Locate every parasitized red blood cell.
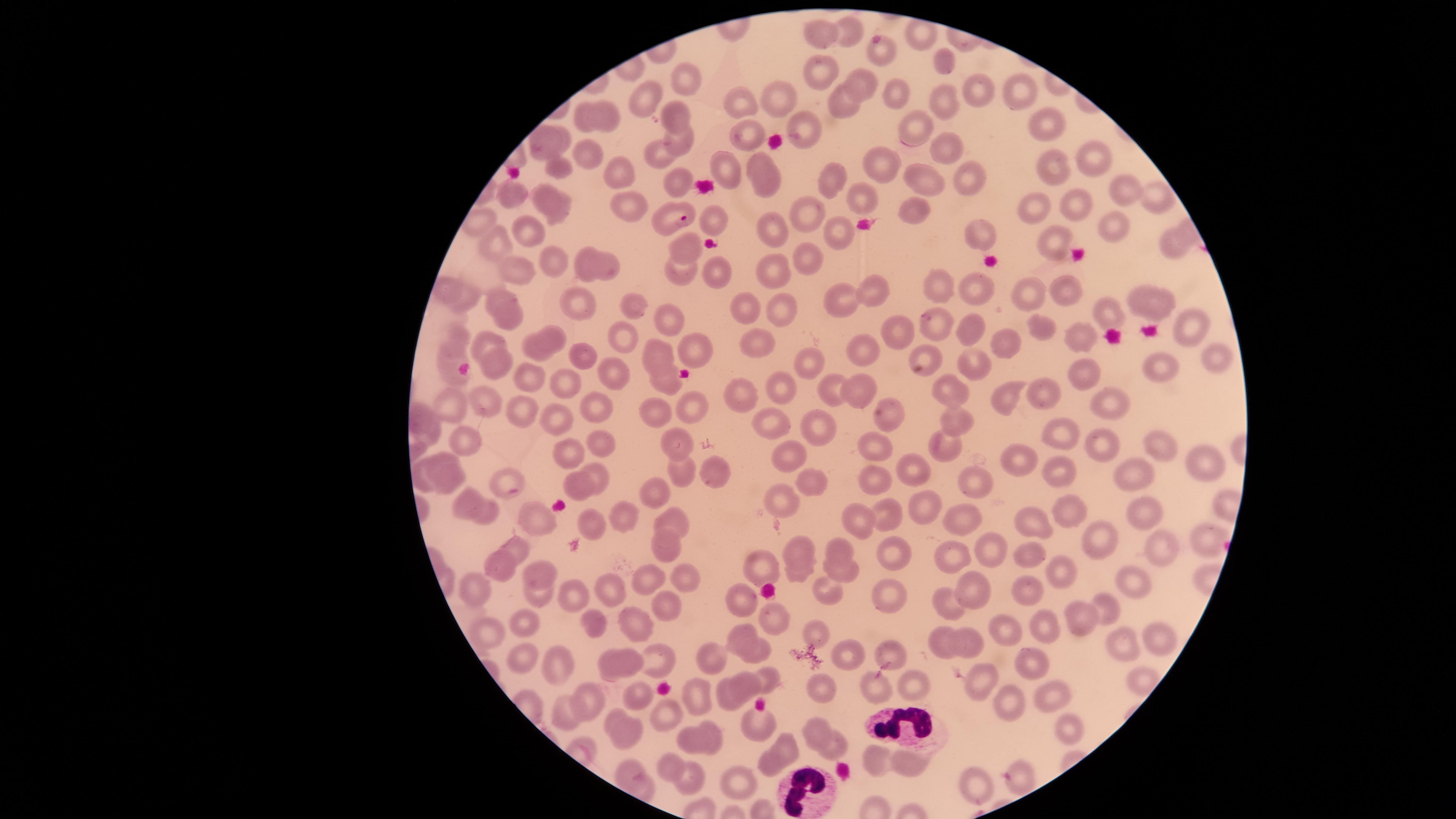
Approximate marker points, in pixels from the top-left corner.
Parasitized red blood cells: (x=668, y=215).

Approximate marker points, in pixels from the top-left corner. White blood cells: (x=901, y=723), (x=806, y=794). Uninfected red blood cells: (x=821, y=32), (x=849, y=35), (x=884, y=56), (x=939, y=62), (x=823, y=72), (x=688, y=77), (x=866, y=84), (x=1017, y=86), (x=973, y=87), (x=896, y=92), (x=645, y=94), (x=776, y=94), (x=745, y=101), (x=946, y=104), (x=846, y=106), (x=670, y=111), (x=582, y=116), (x=611, y=119), (x=917, y=121), (x=1045, y=125), (x=747, y=131), (x=562, y=132), (x=677, y=135), (x=803, y=135), (x=591, y=147), (x=544, y=149), (x=658, y=151), (x=946, y=152), (x=1086, y=152), (x=759, y=160), (x=883, y=167), (x=728, y=168), (x=1055, y=170), (x=622, y=173), (x=562, y=174), (x=833, y=174), (x=976, y=176), (x=925, y=180), (x=683, y=181), (x=768, y=182), (x=1124, y=187), (x=551, y=193), (x=1147, y=193), (x=518, y=194), (x=862, y=201), (x=1081, y=204), (x=623, y=205), (x=915, y=212), (x=808, y=213), (x=1038, y=213), (x=564, y=216), (x=711, y=220), (x=847, y=226), (x=1114, y=228), (x=771, y=229), (x=529, y=231), (x=983, y=238), (x=500, y=241), (x=1172, y=244), (x=1059, y=245), (x=688, y=250), (x=586, y=255), (x=548, y=256), (x=813, y=262), (x=607, y=271), (x=680, y=271), (x=518, y=273), (x=717, y=274), (x=771, y=275), (x=938, y=283), (x=981, y=289), (x=1065, y=289), (x=877, y=291), (x=500, y=293), (x=1034, y=293), (x=469, y=298), (x=1142, y=298), (x=1168, y=303), (x=851, y=304), (x=580, y=308), (x=742, y=308), (x=635, y=310), (x=779, y=311), (x=517, y=312), (x=1111, y=314), (x=670, y=317), (x=969, y=328), (x=1042, y=328), (x=1188, y=328), (x=934, y=329), (x=890, y=334), (x=558, y=335), (x=1082, y=335), (x=629, y=336), (x=458, y=341), (x=488, y=341), (x=1004, y=343), (x=763, y=345), (x=537, y=346), (x=705, y=350), (x=653, y=352), (x=929, y=353), (x=579, y=354), (x=861, y=354), (x=502, y=356), (x=808, y=358), (x=1218, y=362), (x=974, y=365), (x=1161, y=367), (x=449, y=368), (x=618, y=373), (x=528, y=374), (x=1086, y=381), (x=569, y=382), (x=665, y=383), (x=783, y=387), (x=945, y=388), (x=830, y=389), (x=858, y=390), (x=742, y=396), (x=1009, y=396), (x=1045, y=397), (x=480, y=399), (x=1112, y=404), (x=455, y=405), (x=597, y=405), (x=694, y=407), (x=659, y=409), (x=523, y=411), (x=556, y=413), (x=955, y=417), (x=889, y=418), (x=423, y=419), (x=772, y=422), (x=817, y=424), (x=1069, y=435), (x=941, y=438), (x=674, y=439), (x=469, y=441), (x=603, y=441), (x=873, y=443), (x=1097, y=443), (x=1159, y=449), (x=572, y=452), (x=783, y=454), (x=443, y=458), (x=1203, y=459), (x=1022, y=465), (x=919, y=467), (x=677, y=468), (x=1057, y=468), (x=1137, y=470), (x=419, y=474), (x=589, y=474), (x=714, y=475), (x=873, y=478), (x=976, y=481), (x=445, y=483), (x=811, y=483), (x=513, y=484), (x=582, y=488), (x=654, y=491), (x=465, y=501), (x=780, y=502), (x=885, y=511), (x=929, y=511), (x=1145, y=511), (x=1067, y=513), (x=490, y=515), (x=616, y=515), (x=964, y=517), (x=535, y=518), (x=858, y=518), (x=672, y=519), (x=1035, y=525), (x=590, y=528), (x=1098, y=538), (x=1207, y=540), (x=660, y=545), (x=837, y=546), (x=521, y=547), (x=802, y=547), (x=994, y=548), (x=1160, y=548), (x=894, y=552), (x=959, y=555), (x=1033, y=558), (x=763, y=564), (x=500, y=569), (x=842, y=572), (x=533, y=574), (x=799, y=574), (x=683, y=576), (x=646, y=577), (x=1064, y=580), (x=1125, y=580), (x=827, y=587), (x=467, y=588), (x=606, y=592), (x=888, y=592), (x=973, y=594), (x=1027, y=596), (x=537, y=598), (x=571, y=599), (x=739, y=600), (x=945, y=601), (x=665, y=603), (x=1109, y=607), (x=1082, y=619), (x=528, y=621), (x=638, y=621), (x=596, y=622), (x=774, y=623), (x=488, y=629), (x=1154, y=630), (x=815, y=631), (x=1010, y=631), (x=1048, y=632), (x=745, y=638), (x=943, y=638), (x=966, y=638), (x=1127, y=645), (x=887, y=651), (x=522, y=652), (x=762, y=653), (x=657, y=654), (x=705, y=655), (x=851, y=656), (x=632, y=660), (x=1030, y=661), (x=558, y=665), (x=608, y=665), (x=912, y=677), (x=765, y=680), (x=877, y=681), (x=983, y=682), (x=747, y=686), (x=822, y=690), (x=1044, y=692), (x=697, y=694), (x=632, y=695), (x=593, y=699), (x=725, y=699), (x=1012, y=703), (x=559, y=707), (x=615, y=713), (x=667, y=717), (x=814, y=725), (x=710, y=727), (x=1068, y=730), (x=632, y=731), (x=758, y=731), (x=691, y=741), (x=787, y=745), (x=832, y=747), (x=875, y=761), (x=769, y=763), (x=912, y=765), (x=670, y=767), (x=628, y=770), (x=689, y=778), (x=973, y=782), (x=740, y=783). Smartphone photograph through the microscope eyepiece. Image is 1456×819 pixels. The visible region is circular. Giemsa-stained preparation. Single field of view. Thin blood film. Species: Plasmodium falciparum.